Outline each blood parasite and name the species.
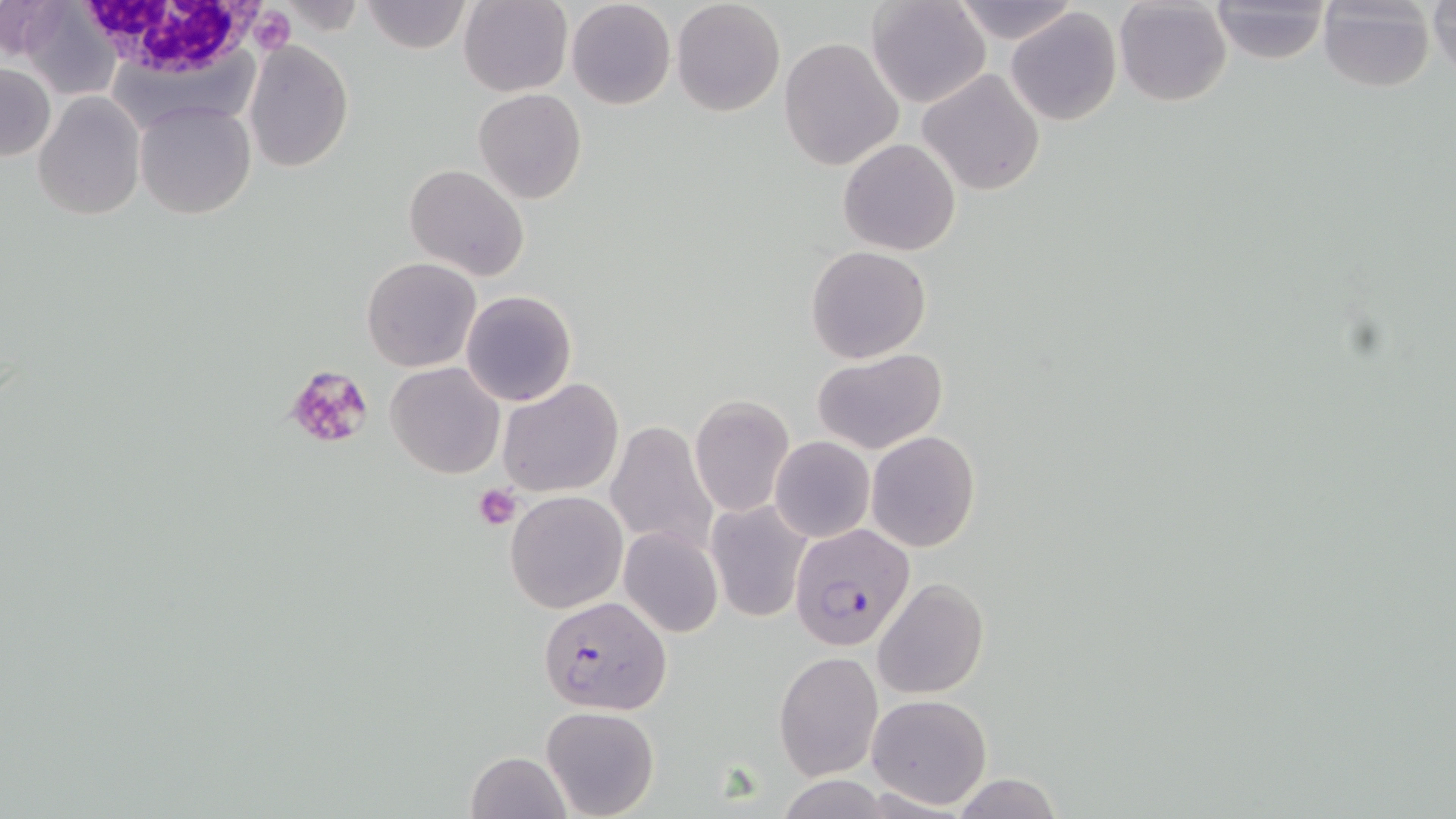
Approximate bounding boxes as (x1, y1, x2, y2) in pixels.
Plasmodium falciparum-infected red blood cells: (790, 524, 917, 652), (538, 596, 671, 715).
No Plasmodium ovale, Plasmodium malariae, Plasmodium vivax, Babesia divergens, or Trypanosoma brucei observed.

Summary:
  - White blood cell locations: (76, 0, 264, 81)
  - Platelet locations: (247, 7, 296, 54), (288, 367, 372, 446), (476, 485, 522, 530)
  - Uninfected red blood cell locations: (360, 0, 470, 54), (868, 0, 993, 109), (948, 0, 1079, 44), (1208, 0, 1332, 64), (1428, 0, 1456, 76), (0, 1, 66, 60), (460, 1, 573, 97), (567, 1, 676, 111), (671, 1, 784, 117), (1114, 1, 1231, 107), (1317, 2, 1435, 92), (20, 5, 122, 99), (1005, 8, 1122, 127), (779, 36, 904, 172), (245, 41, 354, 171), (0, 63, 55, 161), (917, 68, 1046, 195), (473, 89, 588, 205), (34, 92, 145, 221), (133, 100, 257, 220), (839, 138, 962, 256), (404, 163, 529, 281), (806, 246, 932, 364), (361, 257, 482, 373), (460, 290, 577, 406), (813, 349, 948, 457), (385, 361, 504, 478), (498, 377, 622, 498), (688, 395, 795, 516), (607, 419, 720, 558), (866, 430, 980, 551), (771, 436, 874, 542), (504, 491, 628, 613), (707, 501, 811, 623), (618, 527, 723, 639), (873, 578, 989, 699), (774, 650, 883, 779), (866, 693, 992, 810), (541, 706, 658, 819), (466, 751, 572, 818), (953, 775, 1063, 818)
  - Slide-level diagnosis: Plasmodium falciparum
  - Field of view: single
  - Stain: May-Grünwald-Giemsa
  - Preparation: thin blood film
  - Modality: light microscopy
  - Magnification: 1000x
  - Image size: 1456×819 pixels